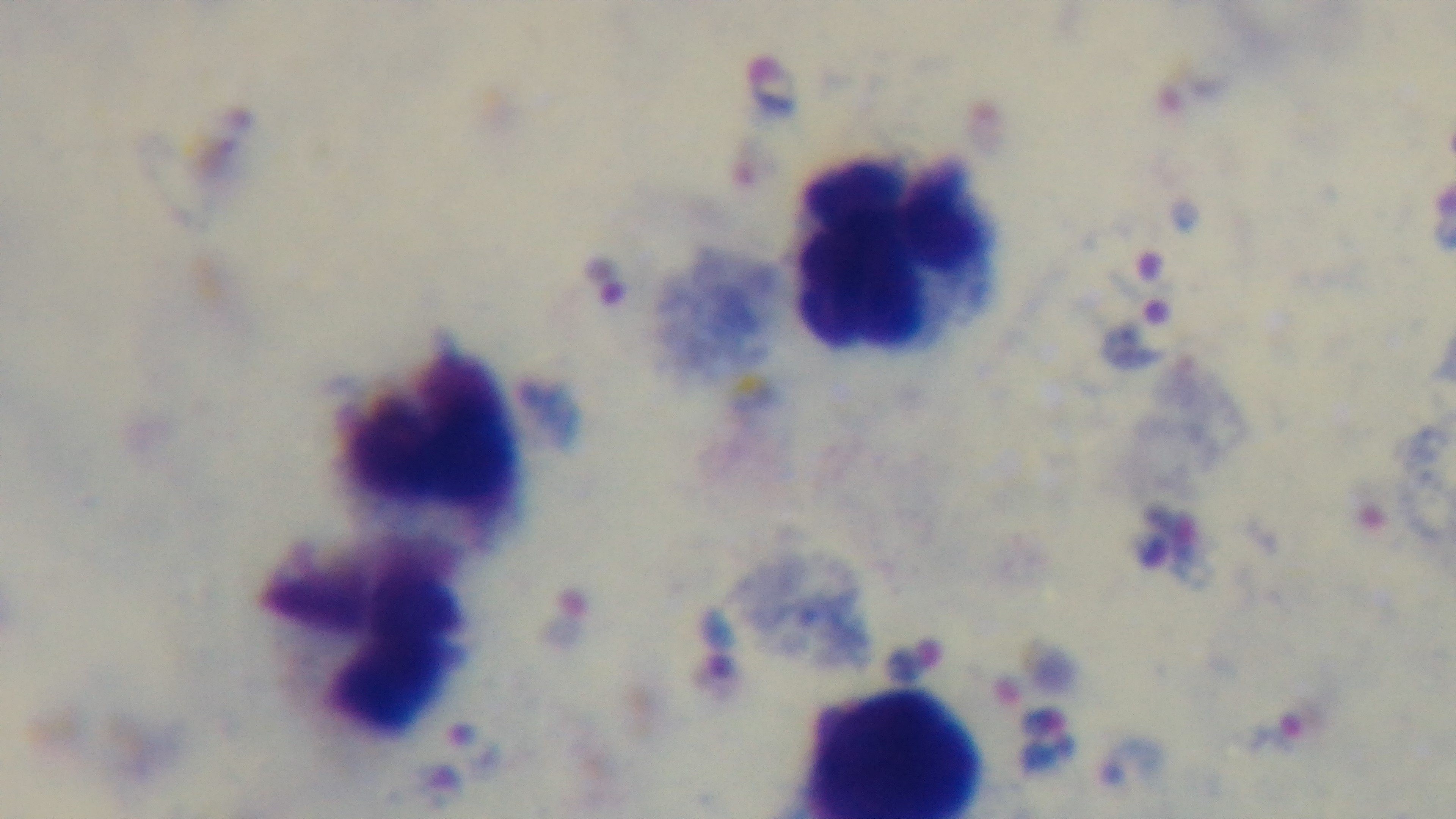
capture = mounted 4K digital camera
preparation = thick smear
malaria status = infected
stain = Giemsa
field of view = single
modality = light microscopy
objective = 100x oil immersion